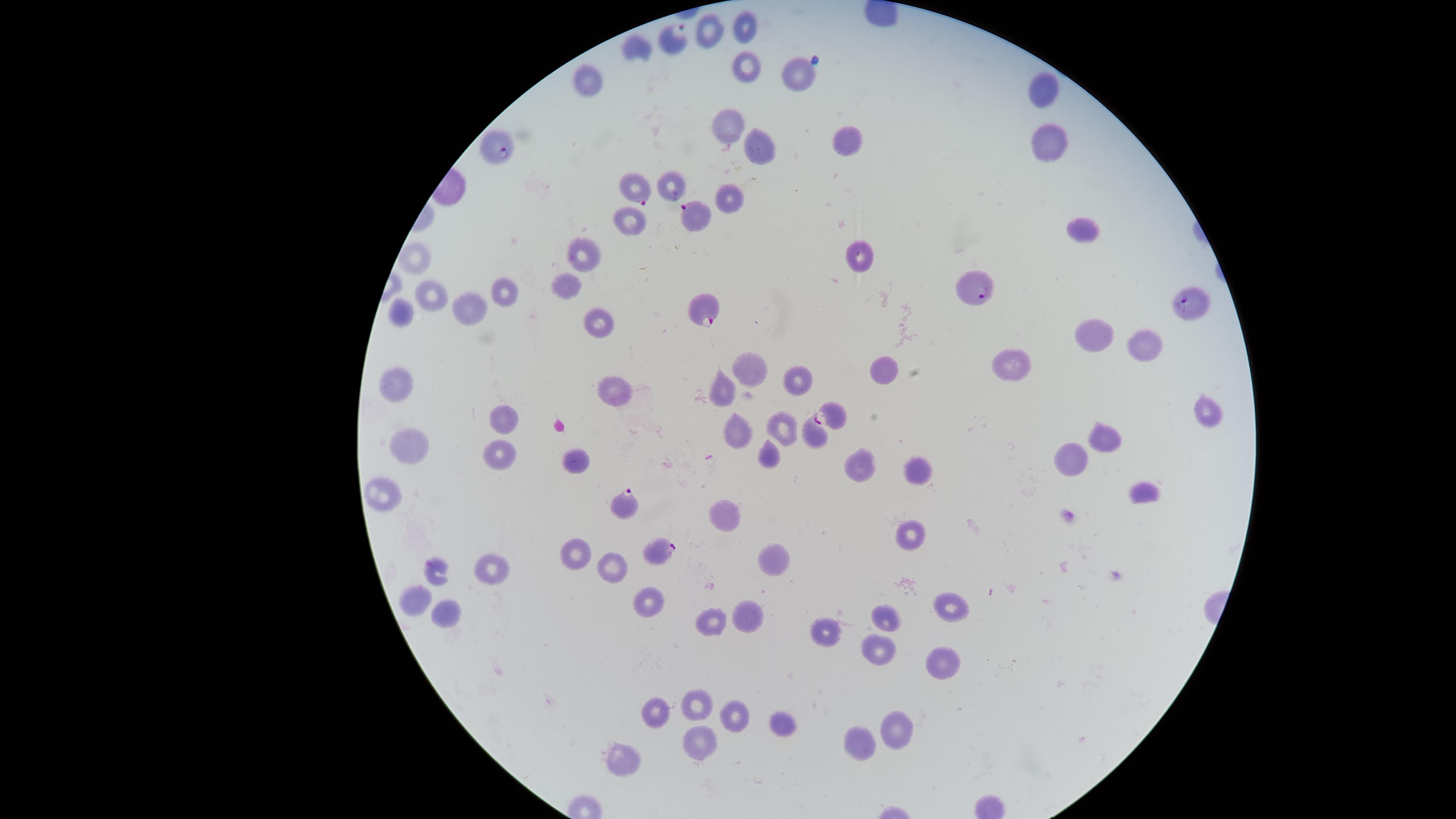
Approximate marker points as {x, y} in pixels.
Summary:
  - Uninfected RBCs: {740, 25}, {718, 33}, {634, 45}, {746, 67}, {793, 70}, {591, 84}, {1043, 94}, {731, 126}, {846, 140}, {1048, 142}, {761, 153}, {671, 186}, {730, 200}, {630, 222}, {1082, 226}, {859, 257}, {414, 258}, {583, 259}, {573, 280}, {505, 291}, {429, 292}, {468, 309}, {404, 318}, {596, 324}, {1088, 334}, {1145, 338}, {1010, 364}, {890, 370}, {747, 373}, {796, 378}, {399, 389}, {615, 389}, {724, 394}, {1202, 411}, {503, 418}, {736, 427}, {783, 427}, {814, 433}, {1103, 435}, {412, 447}, {498, 456}, {772, 456}, {578, 460}, {1072, 460}, {915, 470}, {860, 471}, {1150, 490}, {384, 493}, {732, 515}, {907, 536}, {577, 556}, {772, 562}, {488, 568}, {436, 569}, {617, 569}, {419, 596}, {653, 603}, {950, 609}, {452, 610}, {890, 616}, {745, 620}, {710, 625}, {827, 633}, {878, 649}, {944, 663}, {705, 704}, {653, 712}, {734, 713}, {897, 725}, {783, 726}, {861, 744}, {698, 745}, {623, 759}
  - Parasitized RBCs: {677, 38}, {495, 149}, {636, 188}, {696, 219}, {975, 289}, {1191, 301}, {704, 312}, {828, 415}, {628, 506}, {657, 549}
  - Preparation: thin blood smear
  - Stain: Giemsa
  - Field of view: single
  - Presence: malaria parasites seen
  - Capture: smartphone photograph through the microscope eyepiece
  - Visible region: circular
  - Species: Plasmodium falciparum
  - Image size: 1456×819 pixels